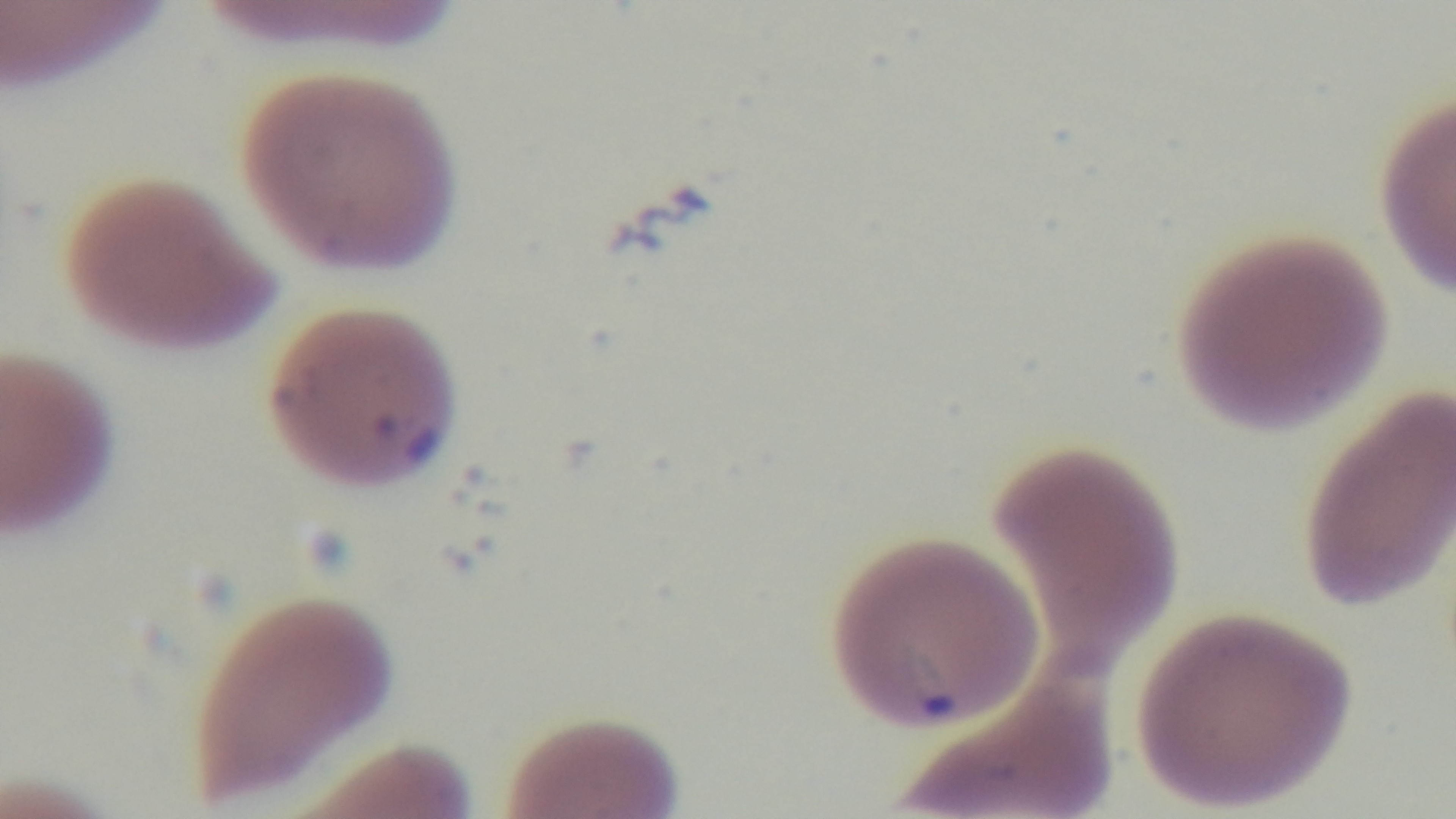

malaria_status: infected
capture: mounted 4K digital camera
preparation: thin smear
modality: light microscopy
stain: Giemsa
objective: 100x oil immersion
field_of_view: single